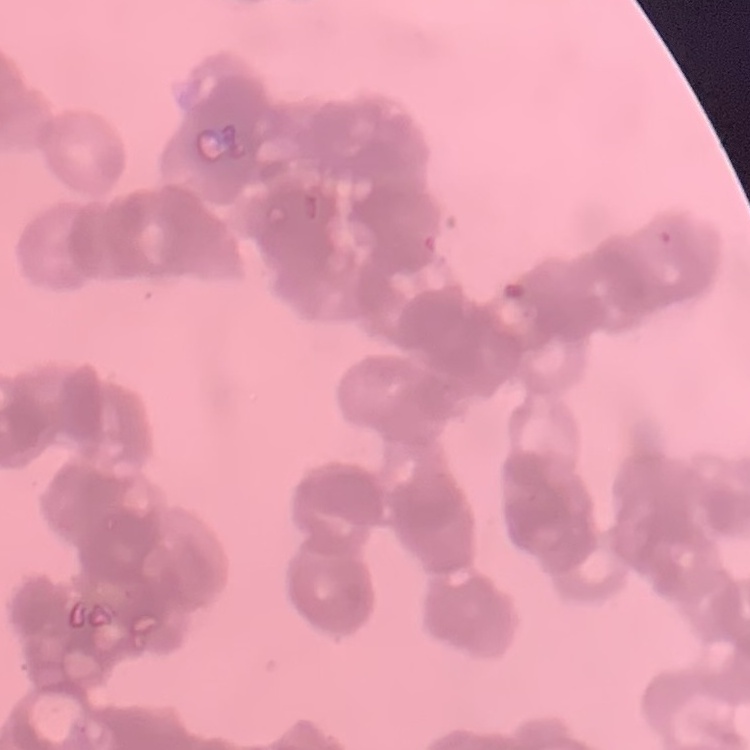
Summary:
  - Red blood cell morphology: rouleaux formation
  - Image type: one tile cut from a larger photomicrograph
  - Stain: Field's or Giemsa
  - Preparation: thin blood smear